Identify the blood parasite species.
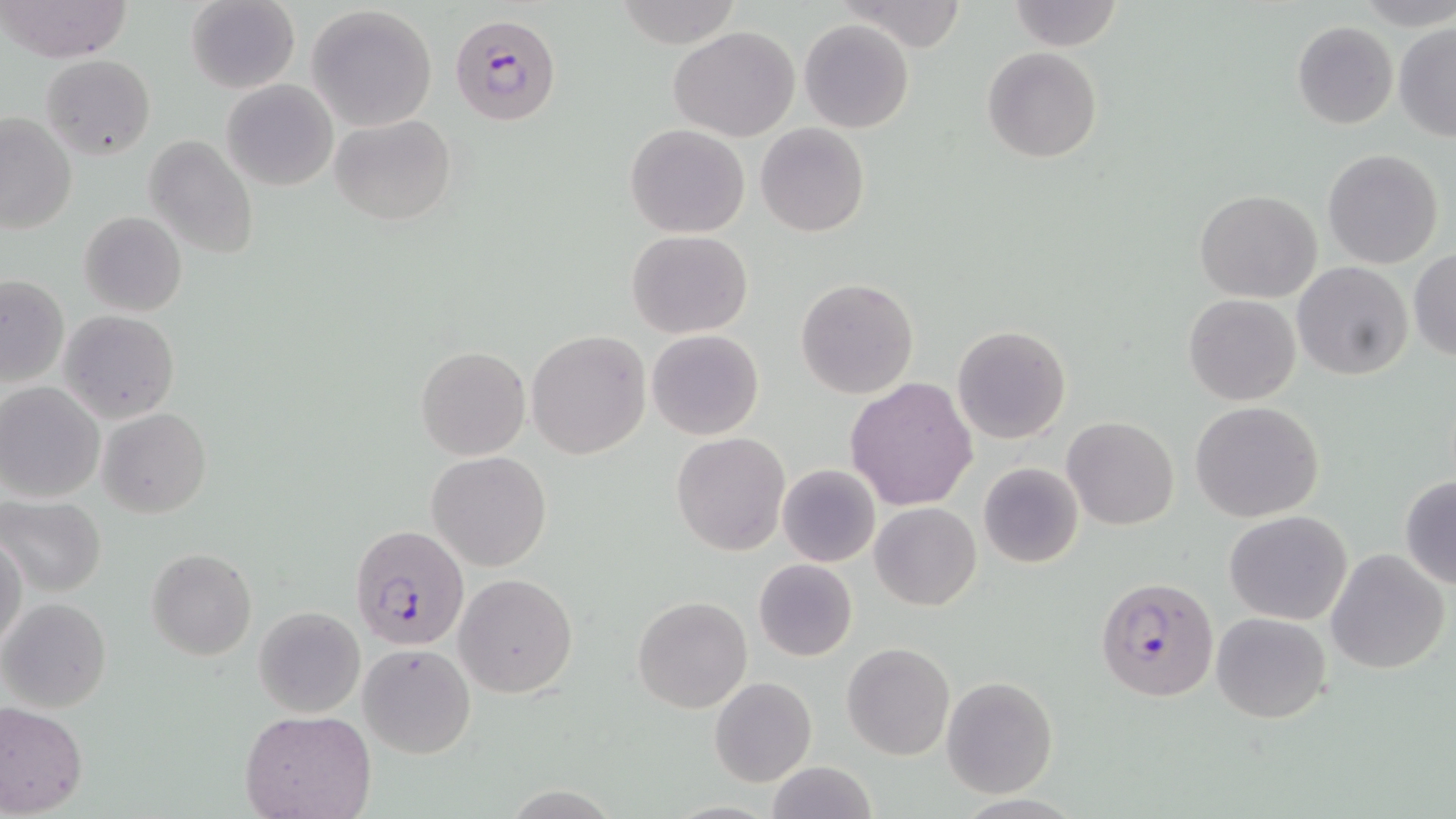
Plasmodium falciparum.

Approximate bounding boxes as named x1/y1/x2/y2 corners in pixels. Plasmodium falciparum-infected red blood cell locations: (x1=450, y1=13, x2=563, y2=123), (x1=349, y1=524, x2=468, y2=650), (x1=1094, y1=577, x2=1215, y2=702). Uninfected red blood cell locations: (x1=1, y1=0, x2=131, y2=65), (x1=612, y1=0, x2=746, y2=49), (x1=836, y1=0, x2=970, y2=51), (x1=1007, y1=0, x2=1125, y2=51), (x1=184, y1=1, x2=299, y2=92), (x1=306, y1=5, x2=438, y2=131), (x1=798, y1=19, x2=916, y2=133), (x1=1393, y1=20, x2=1456, y2=142), (x1=1292, y1=21, x2=1398, y2=130), (x1=668, y1=26, x2=801, y2=142), (x1=982, y1=47, x2=1103, y2=164), (x1=40, y1=54, x2=155, y2=159), (x1=221, y1=79, x2=339, y2=190), (x1=1, y1=112, x2=76, y2=235), (x1=330, y1=114, x2=456, y2=225), (x1=755, y1=122, x2=870, y2=237), (x1=625, y1=123, x2=749, y2=238), (x1=143, y1=135, x2=260, y2=259), (x1=1322, y1=148, x2=1444, y2=269), (x1=1196, y1=190, x2=1321, y2=303), (x1=79, y1=211, x2=186, y2=317), (x1=625, y1=230, x2=753, y2=339), (x1=1408, y1=249, x2=1456, y2=363), (x1=1292, y1=263, x2=1412, y2=382), (x1=0, y1=274, x2=69, y2=387), (x1=795, y1=277, x2=918, y2=399), (x1=1183, y1=294, x2=1301, y2=406), (x1=59, y1=309, x2=179, y2=423), (x1=952, y1=324, x2=1071, y2=443), (x1=646, y1=329, x2=764, y2=440), (x1=526, y1=331, x2=651, y2=460), (x1=415, y1=347, x2=529, y2=461), (x1=845, y1=376, x2=978, y2=511), (x1=0, y1=384, x2=103, y2=503), (x1=1190, y1=400, x2=1324, y2=522), (x1=97, y1=407, x2=212, y2=517), (x1=1062, y1=416, x2=1179, y2=530), (x1=672, y1=432, x2=790, y2=557), (x1=428, y1=451, x2=551, y2=571), (x1=978, y1=462, x2=1085, y2=568), (x1=776, y1=464, x2=881, y2=568), (x1=1399, y1=475, x2=1456, y2=588), (x1=0, y1=496, x2=106, y2=597), (x1=871, y1=502, x2=981, y2=610), (x1=1224, y1=511, x2=1352, y2=625), (x1=0, y1=530, x2=27, y2=656), (x1=147, y1=547, x2=258, y2=661), (x1=1327, y1=549, x2=1450, y2=676), (x1=752, y1=558, x2=857, y2=662), (x1=455, y1=573, x2=577, y2=697), (x1=633, y1=596, x2=751, y2=713), (x1=1, y1=598, x2=112, y2=713), (x1=253, y1=606, x2=365, y2=718), (x1=1211, y1=612, x2=1330, y2=723), (x1=358, y1=642, x2=475, y2=758), (x1=842, y1=642, x2=956, y2=762), (x1=709, y1=677, x2=816, y2=787), (x1=941, y1=677, x2=1058, y2=797), (x1=0, y1=702, x2=88, y2=817), (x1=241, y1=711, x2=375, y2=819), (x1=764, y1=761, x2=876, y2=819). Single field of view. May-Grünwald-Giemsa-stained preparation. Thin blood smear. Optical microscopy. Image is 1456×819 pixels. Captured at 1000x magnification.